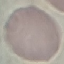
result = no malaria parasites seen
preparation = thin smear
image type = cell patch, automatically extracted from a larger field of view and resized to 64 × 64 pixels
stain = Giemsa
capture = smartphone camera at the microscope eyepiece